Locate platelets.
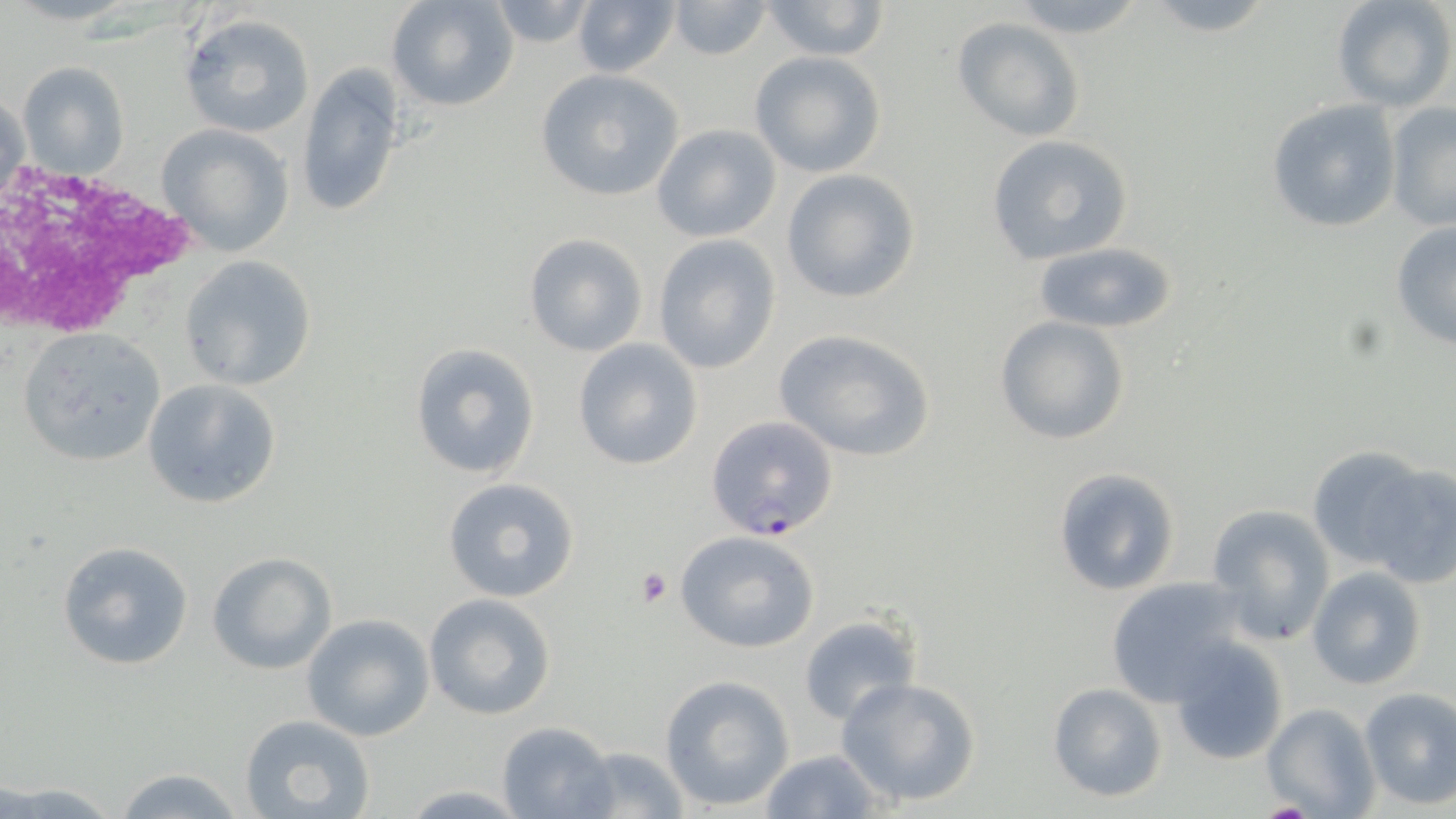
Approximate bounding boxes as (x1, y1, x2, y2) in pixels.
Platelets: (635, 568, 672, 608), (1258, 801, 1317, 817).

slide-level diagnosis = Plasmodium falciparum
stain = May-Grünwald-Giemsa
preparation = thin blood film
field of view = single
magnification = 1000x
modality = light microscopy
uninfected red blood cell locations = approximate bounding boxes as (x1, y1, x2, y2) in pixels: (388, 0, 518, 111), (1139, 0, 1280, 40), (1330, 0, 1454, 114), (571, 1, 681, 78), (666, 1, 775, 62), (761, 1, 889, 61), (999, 1, 1152, 38), (485, 2, 600, 49), (178, 13, 315, 138), (953, 16, 1084, 141), (748, 51, 887, 177), (18, 62, 130, 178), (297, 65, 404, 217), (534, 71, 684, 202), (2, 86, 29, 209), (1266, 99, 1402, 234), (1384, 102, 1455, 233), (156, 123, 296, 257), (650, 123, 782, 243), (985, 135, 1135, 265), (780, 169, 921, 304), (1389, 220, 1456, 351), (522, 233, 648, 357), (652, 235, 782, 375), (1031, 242, 1180, 334), (177, 255, 316, 391), (993, 316, 1133, 445), (18, 327, 167, 466), (773, 329, 936, 461), (572, 337, 705, 470), (409, 343, 541, 479), (141, 378, 282, 509), (1307, 446, 1439, 575), (1363, 462, 1456, 587), (1052, 467, 1180, 597), (441, 476, 580, 603), (1204, 503, 1337, 647), (674, 530, 821, 653), (58, 540, 193, 669), (207, 551, 337, 674), (1307, 566, 1427, 689), (1103, 577, 1253, 706), (424, 593, 556, 720), (301, 614, 435, 741), (797, 614, 920, 725), (818, 626, 966, 772), (1169, 638, 1290, 765), (659, 675, 794, 811), (837, 676, 981, 808), (1047, 682, 1168, 803), (1358, 687, 1456, 809), (1263, 702, 1380, 818), (241, 713, 378, 819), (496, 721, 618, 819), (569, 746, 690, 818), (758, 749, 885, 819), (110, 766, 250, 819), (3, 781, 123, 818), (396, 785, 531, 816)
image size = 1456×819 pixels
white blood cell locations = approximate bounding boxes as (x1, y1, x2, y2) in pixels: (0, 161, 195, 338)
Plasmodium falciparum-infected red blood cell locations = approximate bounding boxes as (x1, y1, x2, y2) in pixels: (704, 415, 839, 540)